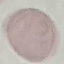
Summary:
  - Result: negative for malaria parasites
  - Preparation: thin smear
  - Image type: automatically extracted cell patch, resized to 64 × 64 pixels
  - Stain: Giemsa
  - Capture: smartphone through the microscope eyepiece